Identify the parasite.
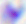

Toxoplasma gondii.

modality = micrograph
magnification = 400x